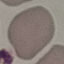

malaria_status: uninfected
capture: smartphone through the microscope eyepiece
image_type: cell patch, automatically extracted from a larger field of view and resized to 64 × 64 pixels
preparation: thin blood film
stain: Giemsa